State which cell type is depicted.
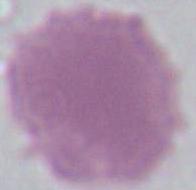

This is an erythrocyte.

Summary:
  - Magnification: 1000x
  - Modality: photomicrograph